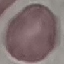
Summary:
  - Result: no malaria parasites detected
  - Preparation: thin blood smear
  - Capture: smartphone through the microscope eyepiece
  - Image type: cell patch, automatically extracted from a larger field of view and resized to 64 × 64 pixels
  - Stain: Giemsa